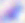
Toxoplasma gondii is seen. 400x magnification. Photomicrograph.